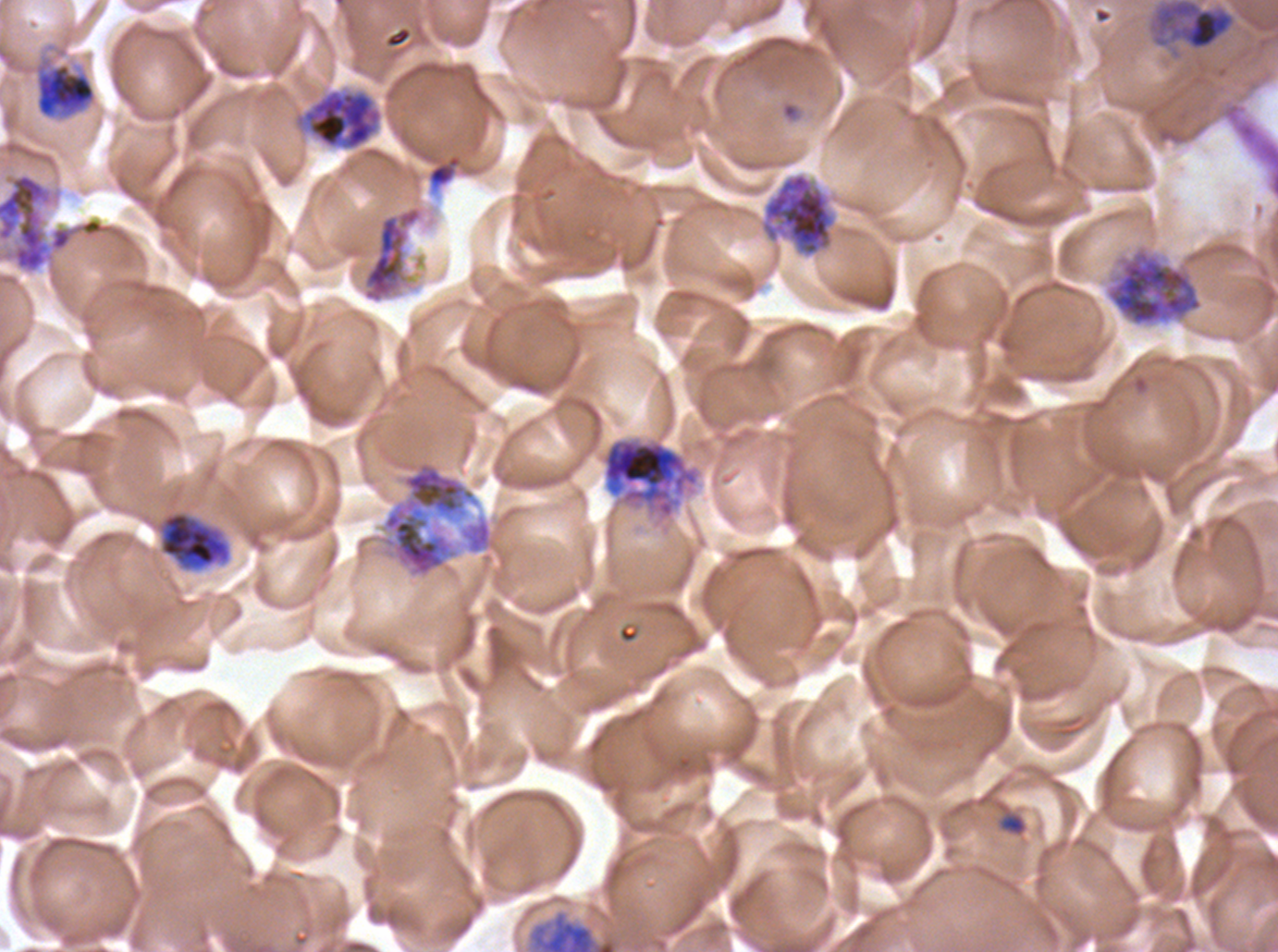 Approximate bounding rectangles given as corner coordinates in pixels from the top-left. Segmenter locations: (x1=0, y1=172, x2=133, y2=274), (x1=763, y1=173, x2=833, y2=256), (x1=360, y1=202, x2=426, y2=305), (x1=1105, y1=246, x2=1204, y2=327), (x1=600, y1=437, x2=701, y2=521), (x1=377, y1=452, x2=481, y2=580). Early schizont locations: (x1=1149, y1=0, x2=1236, y2=52), (x1=32, y1=54, x2=98, y2=122), (x1=301, y1=89, x2=382, y2=151), (x1=132, y1=458, x2=234, y2=575), (x1=531, y1=913, x2=618, y2=951). Ring locations: (x1=998, y1=812, x2=1027, y2=836). Giemsa-stained preparation. Thin blood film. One sub-image of a larger composite. P. falciparum from a patient in The Gambia, cultured ex vivo for 24 to 48 hours. Image is 1278×952 pixels. Life-cycle stages observed: ring, early schizont, segmenter.